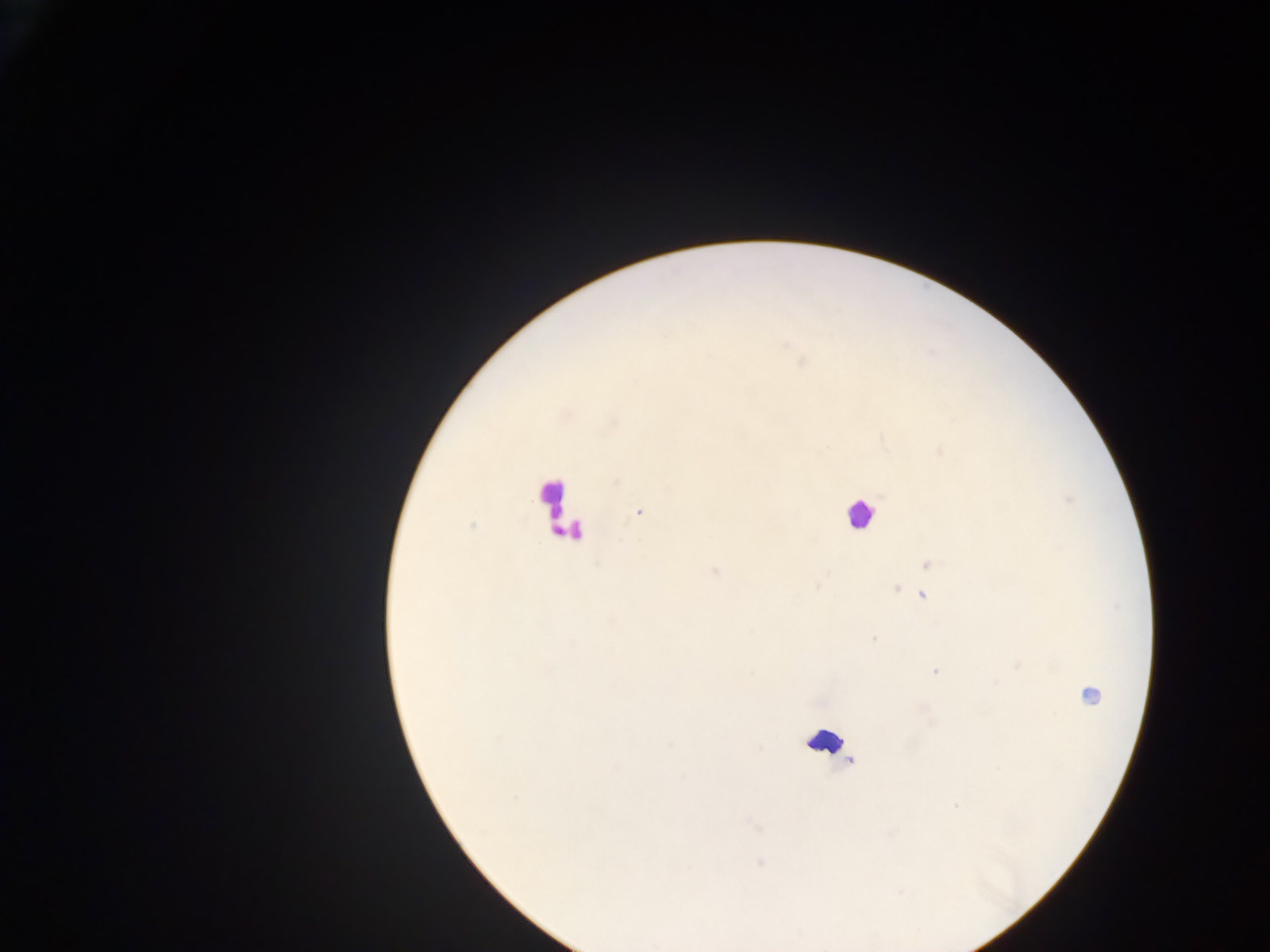

Approximate centers as x y in pixels. Leukocyte locations: 553 499; 859 514; 561 515; 1086 692; 826 742. Malaria parasite locations: 638 512; 473 525; 929 563; 715 571; 816 587; 896 589; 924 596; 873 638; 1018 666; 934 671; 500 739; 516 797; 956 806; 757 826; 760 862. Image is 1270×952 pixels. Photographed through a microscope with a mobile-phone camera. Thick blood film. Sample from Ghana. Single field of view.